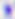

identification = Toxoplasma gondii
modality = micrograph
magnification = 400x